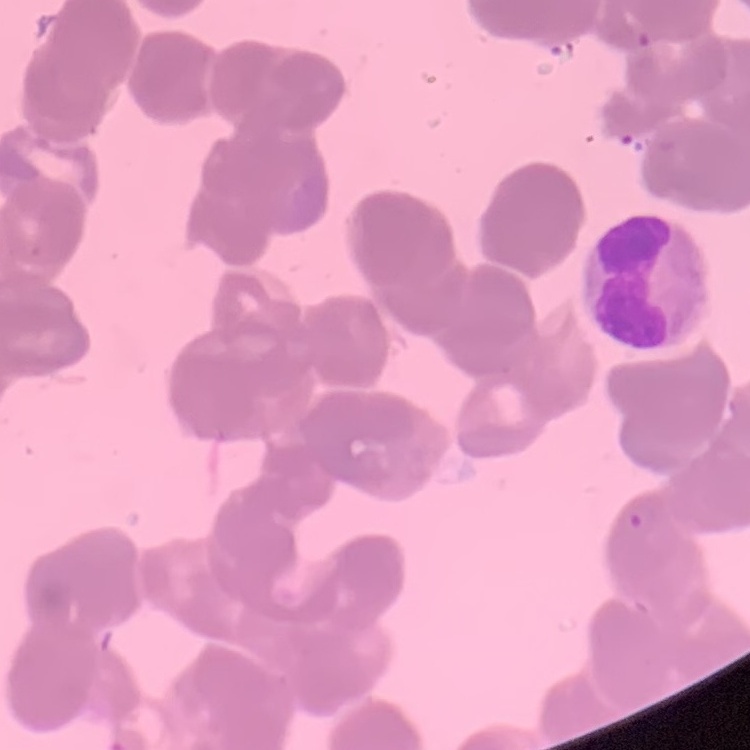
The erythrocytes show rouleaux formation. Thin peripheral smear. Square crop of a larger photomicrograph. Stained with either Field's or Giemsa.